Report the malaria status of this cell.
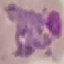
Parasitized.

preparation = thin blood smear
capture = smartphone through the microscope eyepiece
image type = cell patch, automatically extracted from a larger field of view and resized to 64 × 64 pixels
stain = Giemsa